Name the parasite shown.
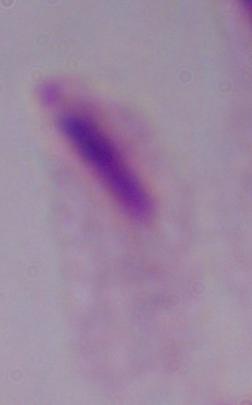
This is a trichomonad.

1000x magnification. Photomicrograph.